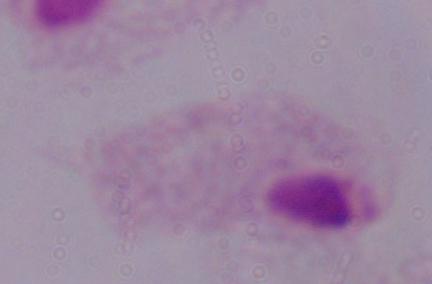
Summary:
  - Magnification: 1000x
  - Modality: micrograph
  - Identification: trichomonad